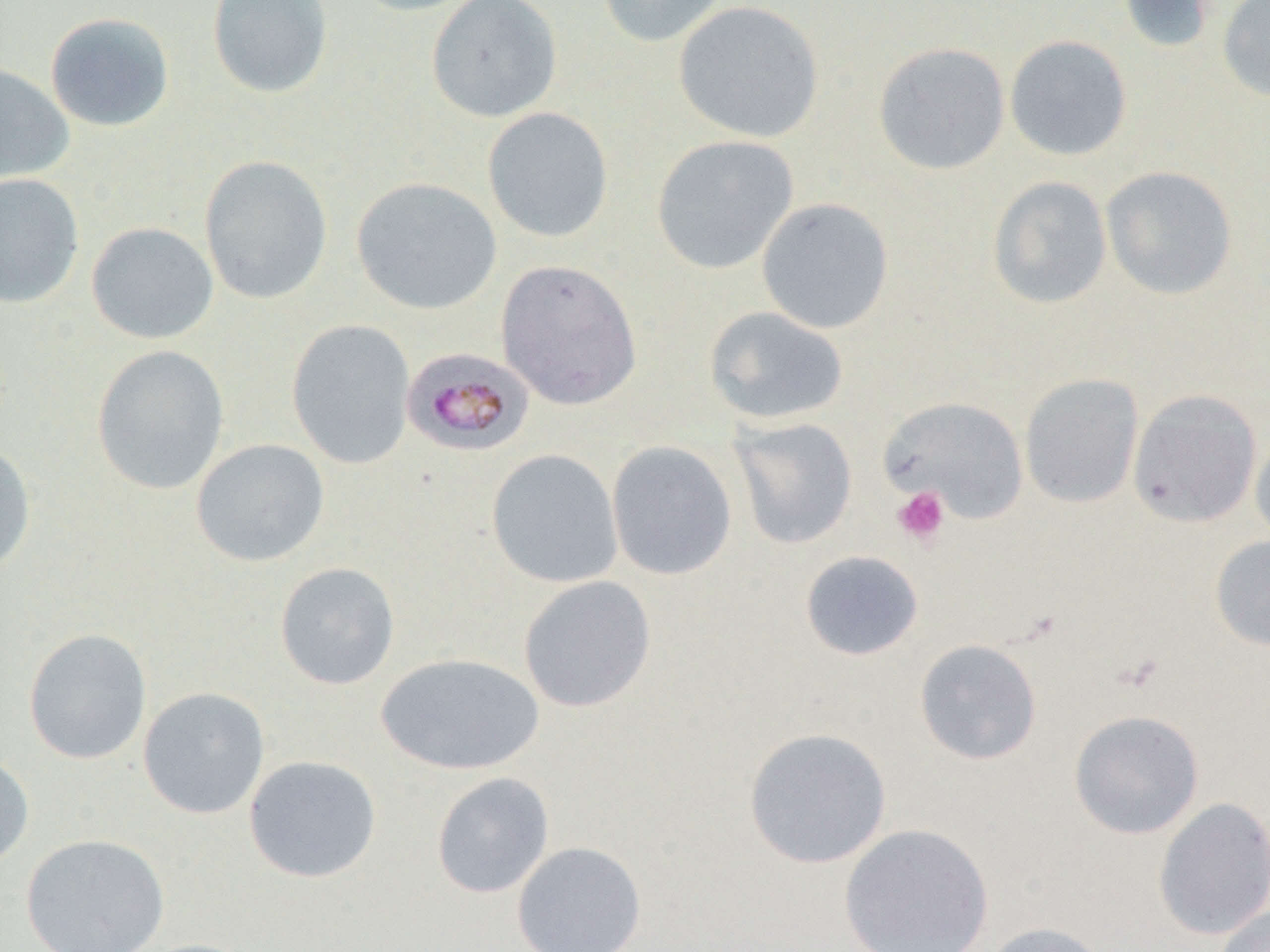 Approximate bounding boxes as (x1,y1)-(x2,y2) corner pairs in pixels. Platelet locations: (893,486)-(950,546). Plasmodium malariae-infected red blood cell locations: (401,347)-(535,457). Uninfected red blood cell locations: (206,0)-(334,100), (346,0)-(487,17), (426,0)-(563,123), (596,0)-(729,47), (1118,0)-(1221,55), (1217,0)-(1270,102), (672,1)-(825,143), (44,12)-(175,132), (1004,35)-(1133,161), (873,41)-(1010,175), (0,62)-(74,185), (482,107)-(614,243), (652,135)-(799,274), (199,154)-(333,304), (1101,166)-(1238,299), (0,172)-(85,310), (988,176)-(1112,309), (351,177)-(501,315), (756,197)-(894,334), (86,221)-(219,344), (495,259)-(642,411), (703,306)-(849,426), (286,319)-(416,469), (90,344)-(231,495), (1019,372)-(1144,508), (1127,389)-(1263,529), (880,396)-(1029,524), (728,417)-(858,549), (1250,428)-(1270,548), (190,439)-(329,567), (0,441)-(36,578), (606,441)-(737,580), (486,449)-(623,588), (1209,535)-(1270,652), (799,550)-(924,661), (274,561)-(401,690), (518,575)-(657,713), (23,628)-(152,764), (914,639)-(1042,765), (375,652)-(545,776), (138,686)-(270,819), (1069,709)-(1205,839), (743,727)-(892,869), (0,750)-(34,872), (244,754)-(382,883), (431,772)-(555,898), (1153,797)-(1270,940), (839,822)-(994,952), (20,833)-(170,952), (511,840)-(646,952), (1214,905)-(1270,952), (981,921)-(1113,952). Slide-level diagnosis: Plasmodium malariae. One field of a larger specimen. Captured at 1000x magnification. Optical microscopy. Thin blood smear. Image is 1270×952 pixels.